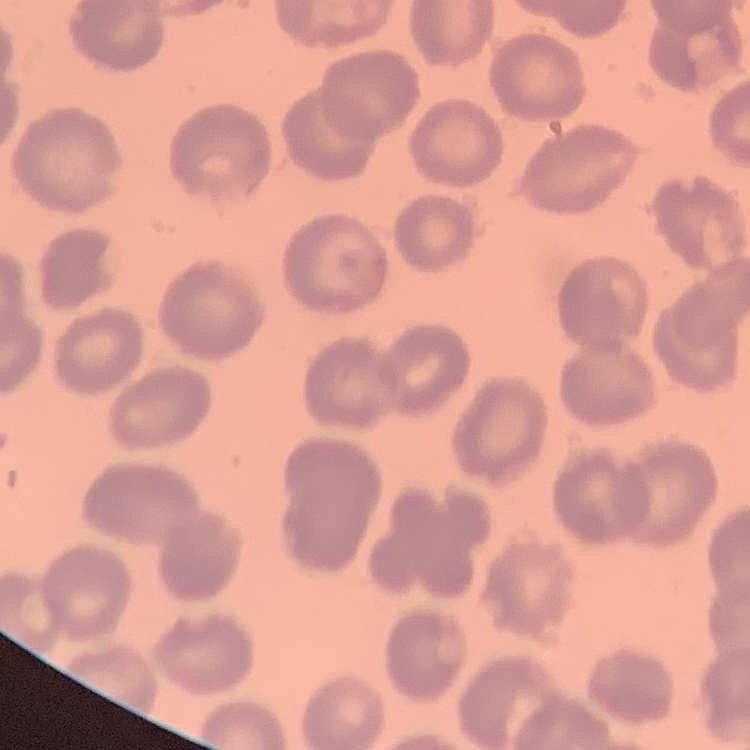

red blood cell morphology = no rouleaux formation
preparation = thin peripheral smear
image type = one tile cut from a larger photomicrograph
stain = Field's or Giemsa